Outline each blood parasite and name the species.
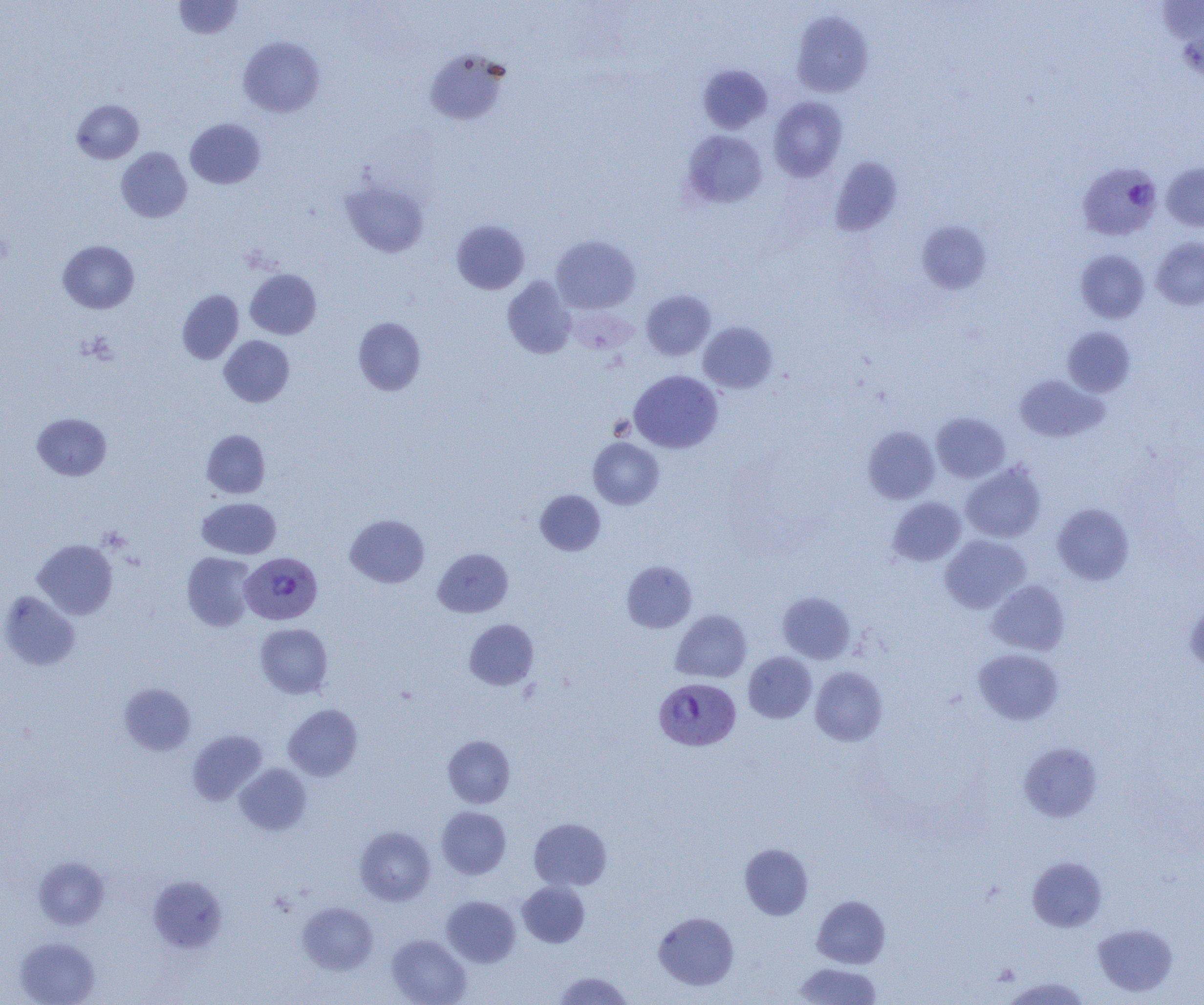

Approximate bounding boxes as [x1, y1, x2, y2] in pixels.
Plasmodium vivax-infected red blood cells: [1077, 162, 1161, 240], [240, 550, 322, 623], [653, 677, 741, 750].
No Plasmodium falciparum, Plasmodium ovale, Plasmodium malariae, Babesia divergens, or Trypanosoma brucei observed.

{
  "slide_level_diagnosis": "Plasmodium vivax",
  "field_of_view": "single",
  "magnification": "1000x",
  "modality": "optical microscopy",
  "uninfected_red_blood_cell_locations": "approximate bounding boxes as [x1, y1, x2, y2] in pixels: [173, 1, 243, 39], [791, 9, 874, 98], [1174, 13, 1204, 85], [238, 36, 325, 117], [424, 48, 511, 126], [697, 64, 773, 134], [768, 96, 848, 181], [72, 99, 144, 163], [185, 118, 266, 189], [681, 130, 767, 209], [116, 147, 192, 222], [829, 156, 904, 237], [1162, 161, 1204, 231], [340, 179, 429, 258], [451, 219, 529, 294], [917, 220, 992, 295], [551, 235, 640, 314], [1152, 237, 1204, 310], [58, 240, 139, 314], [1075, 249, 1150, 323], [245, 268, 322, 339], [502, 276, 577, 359], [177, 290, 243, 364], [641, 290, 715, 360], [353, 317, 426, 395], [699, 322, 777, 393], [1062, 326, 1136, 397], [219, 335, 294, 407], [629, 369, 722, 453], [1014, 374, 1107, 443], [32, 412, 111, 481], [931, 412, 1010, 482], [863, 426, 939, 504], [202, 429, 271, 498], [588, 437, 663, 510], [961, 463, 1046, 542], [535, 490, 605, 555], [888, 497, 966, 566], [197, 498, 281, 559], [1052, 503, 1134, 585], [345, 514, 429, 588], [940, 535, 1031, 613], [33, 539, 118, 619], [433, 547, 513, 618], [182, 552, 256, 631], [621, 560, 696, 633], [987, 580, 1070, 655], [1, 591, 80, 671], [777, 591, 855, 663], [1185, 600, 1204, 674], [670, 609, 751, 683], [464, 619, 539, 690], [255, 623, 332, 698], [974, 649, 1063, 724], [743, 651, 817, 723], [810, 667, 887, 746], [119, 683, 196, 755], [283, 704, 363, 781], [188, 730, 267, 805], [443, 735, 515, 808], [1018, 741, 1103, 823], [235, 763, 311, 835], [437, 806, 511, 879], [529, 817, 612, 890], [355, 827, 435, 905], [740, 844, 813, 919], [33, 857, 109, 929], [1028, 857, 1107, 931], [148, 875, 226, 952], [517, 881, 590, 947], [441, 895, 520, 967], [812, 895, 890, 968], [297, 902, 378, 975], [653, 911, 739, 990], [1092, 923, 1177, 997], [387, 934, 471, 1005], [16, 937, 100, 1005], [793, 962, 881, 1005], [554, 971, 634, 1004], [1002, 976, 1090, 1005]",
  "preparation": "thin blood film",
  "image_size": "1204×1005 pixels"
}